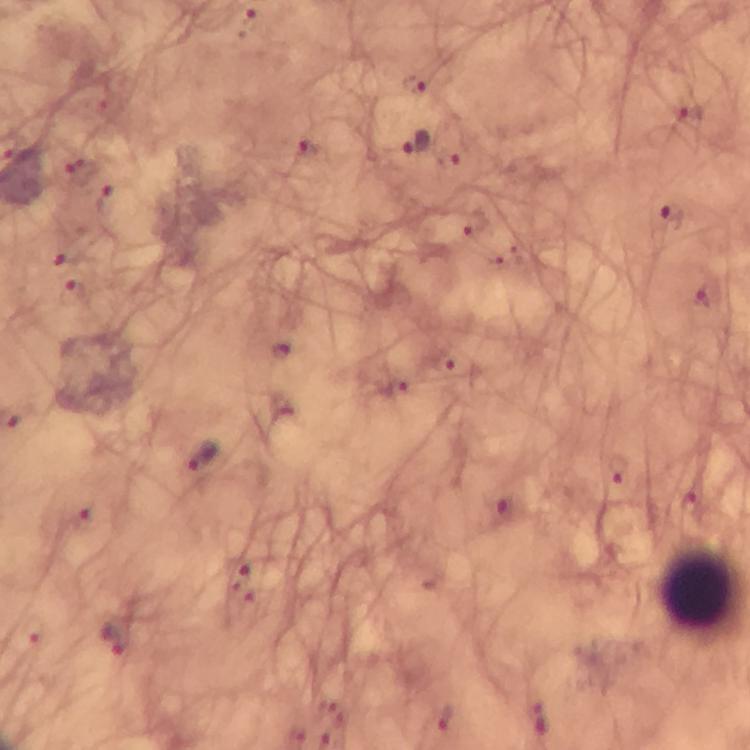
{
  "capture": "smartphone camera through the microscope",
  "preparation": "thick blood smear",
  "malaria_parasite_locations": "approximate centers as {x, y} in pixels: {250, 22}, {414, 85}, {688, 113}, {414, 145}, {308, 155}, {81, 173}, {107, 196}, {674, 216}, {73, 294}, {709, 300}, {457, 365}, {200, 456}, {618, 469}, {501, 508}, {116, 640}",
  "context": "from a diagnostic examination for malaria",
  "magnification": "100x",
  "cropped_from": "a single field of view",
  "stain": "Giemsa",
  "immersion_oil": "used",
  "image_size": "750×750 pixels",
  "leukocyte_locations": "approximate centers as {x, y} in pixels: {701, 589}"
}